Classify this cell by malaria status.
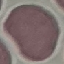

Uninfected.

Automatically extracted cell patch, resized to 64 × 64 pixels. Giemsa stain. Thin blood smear. Acquired by smartphone through the microscope eyepiece.